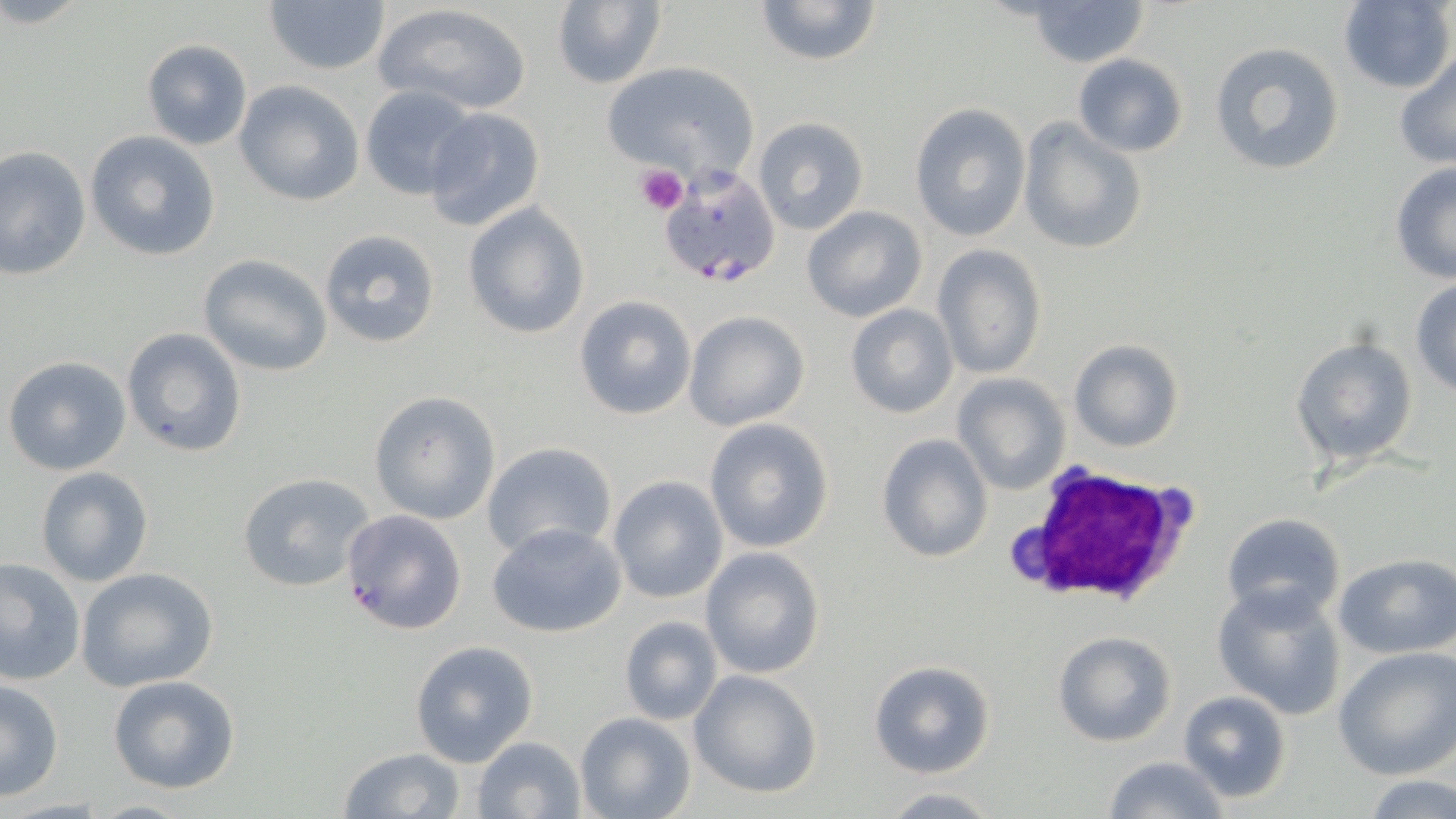

Summary:
  - Coordinate format: approximate bounding boxes as named x1/y1/x2/y2 corners in pixels
  - Uninfected red blood cell locations: (x1=261, y1=0, x2=393, y2=74), (x1=751, y1=0, x2=885, y2=68), (x1=1020, y1=0, x2=1153, y2=68), (x1=1337, y1=0, x2=1454, y2=94), (x1=550, y1=1, x2=665, y2=88), (x1=373, y1=3, x2=533, y2=116), (x1=141, y1=39, x2=252, y2=151), (x1=1208, y1=40, x2=1347, y2=176), (x1=1394, y1=52, x2=1456, y2=168), (x1=1072, y1=53, x2=1188, y2=157), (x1=599, y1=60, x2=760, y2=186), (x1=232, y1=80, x2=365, y2=206), (x1=360, y1=85, x2=481, y2=200), (x1=909, y1=104, x2=1030, y2=242), (x1=422, y1=107, x2=546, y2=232), (x1=1018, y1=117, x2=1148, y2=255), (x1=752, y1=118, x2=869, y2=235), (x1=84, y1=130, x2=222, y2=261), (x1=1, y1=146, x2=91, y2=279), (x1=1389, y1=163, x2=1456, y2=285), (x1=463, y1=202, x2=591, y2=339), (x1=801, y1=205, x2=927, y2=322), (x1=317, y1=230, x2=443, y2=349), (x1=933, y1=245, x2=1047, y2=380), (x1=198, y1=254, x2=332, y2=375), (x1=1410, y1=278, x2=1456, y2=399), (x1=575, y1=295, x2=697, y2=420), (x1=845, y1=304, x2=958, y2=419), (x1=683, y1=310, x2=809, y2=431), (x1=122, y1=327, x2=247, y2=457), (x1=1290, y1=335, x2=1418, y2=467), (x1=1068, y1=339, x2=1184, y2=452), (x1=2, y1=354, x2=133, y2=476), (x1=951, y1=374, x2=1070, y2=494), (x1=368, y1=391, x2=501, y2=524), (x1=704, y1=419, x2=834, y2=554), (x1=875, y1=434, x2=993, y2=564), (x1=481, y1=440, x2=618, y2=560), (x1=36, y1=466, x2=154, y2=586), (x1=237, y1=471, x2=376, y2=592), (x1=607, y1=475, x2=728, y2=604), (x1=340, y1=509, x2=468, y2=636), (x1=1220, y1=512, x2=1347, y2=626), (x1=486, y1=523, x2=628, y2=638), (x1=699, y1=547, x2=825, y2=679), (x1=1334, y1=552, x2=1456, y2=660), (x1=0, y1=556, x2=86, y2=686), (x1=77, y1=566, x2=219, y2=691), (x1=1212, y1=583, x2=1348, y2=719), (x1=619, y1=615, x2=724, y2=725), (x1=1053, y1=632, x2=1176, y2=747), (x1=409, y1=640, x2=538, y2=767), (x1=1334, y1=648, x2=1456, y2=778), (x1=867, y1=659, x2=997, y2=779), (x1=688, y1=670, x2=823, y2=799), (x1=107, y1=675, x2=240, y2=793), (x1=0, y1=680, x2=65, y2=801), (x1=1176, y1=690, x2=1292, y2=804), (x1=574, y1=711, x2=696, y2=819), (x1=472, y1=735, x2=585, y2=818), (x1=335, y1=747, x2=468, y2=819), (x1=1103, y1=756, x2=1229, y2=819), (x1=1361, y1=775, x2=1456, y2=817), (x1=878, y1=788, x2=1004, y2=818)
  - Platelet locations: (x1=635, y1=163, x2=687, y2=214)
  - White blood cell locations: (x1=1005, y1=463, x2=1202, y2=611)
  - Plasmodium falciparum-infected red blood cell locations: (x1=658, y1=165, x2=782, y2=286)
  - Slide-level diagnosis: Plasmodium falciparum
  - Image size: 1456×819 pixels
  - Field of view: single
  - Magnification: 1000x
  - Modality: optical microscopy
  - Preparation: thin blood film
  - Stain: May-Grünwald-Giemsa